Classify this cell by malaria status.
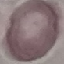
Uninfected.

preparation = thin blood film
stain = Giemsa
capture = smartphone camera at the microscope eyepiece
image type = cell patch, automatically extracted from a larger field of view and resized to 64 × 64 pixels